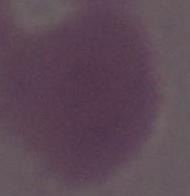
{
  "identification": "erythrocyte",
  "modality": "photomicrograph",
  "magnification": "1000x"
}